Assess this cell for malaria.
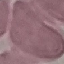
Uninfected.

Photographed with a smartphone camera at the microscope eyepiece. Thin blood smear. Automatically extracted cell patch, resized to 64 × 64 pixels. Giemsa stain.